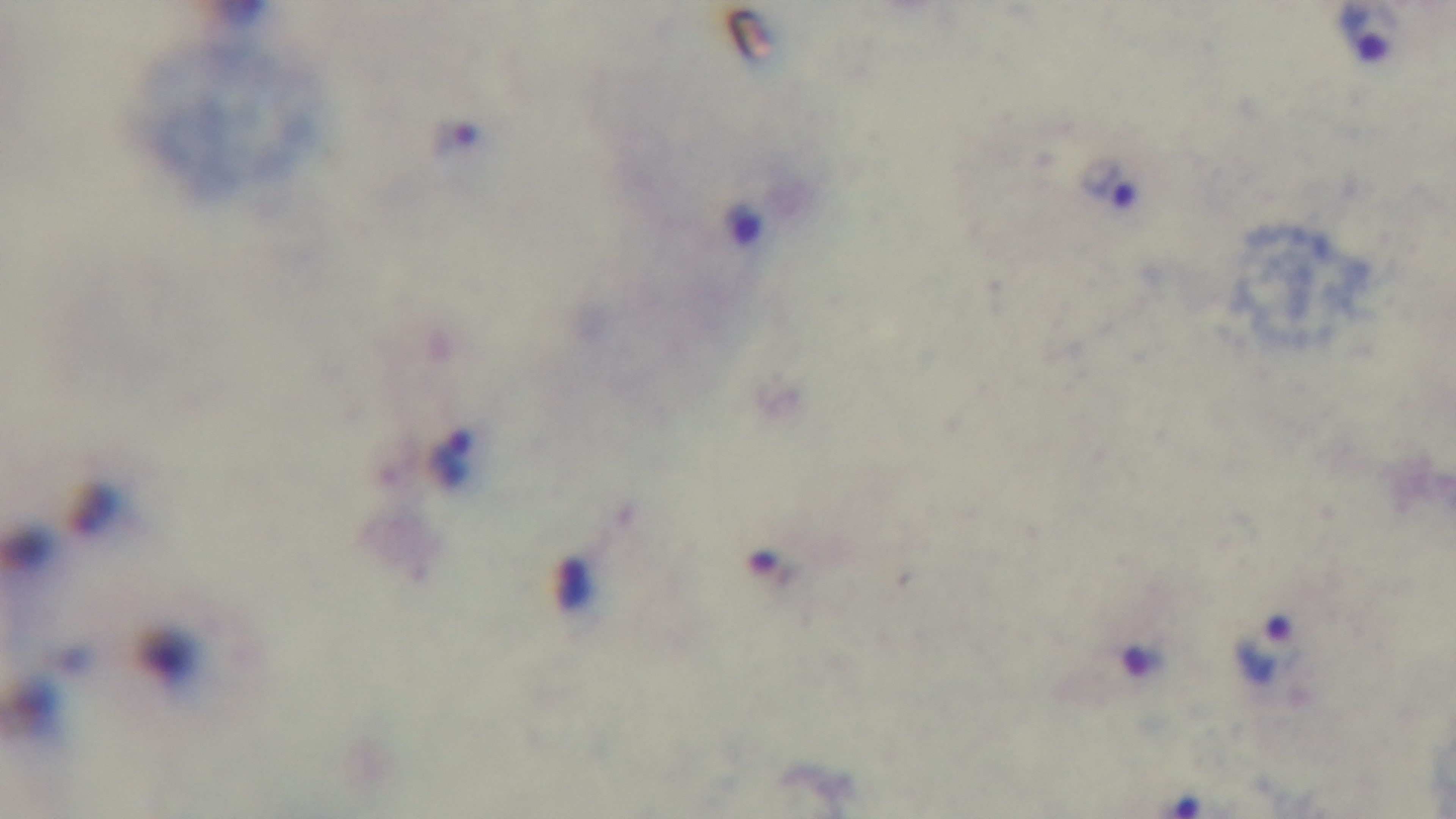 Photomicrograph. One field from the slide. Giemsa-stained. Malaria status: infected. Preparation: thick. Mounted 4K digital camera. 100x oil-immersion objective.